Assess this cell for malaria.
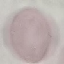
It is uninfected.

Summary:
  - Image type: automatically extracted cell patch, resized to 64 × 64 pixels
  - Stain: Giemsa
  - Preparation: thin blood smear
  - Capture: smartphone camera at the microscope eyepiece